State which cell type is depicted.
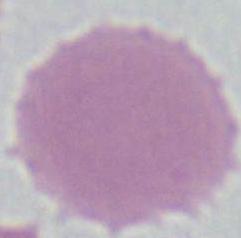

An erythrocyte.

{
  "modality": "photomicrograph",
  "magnification": "1000x"
}